Look for parasitized red blood cells.
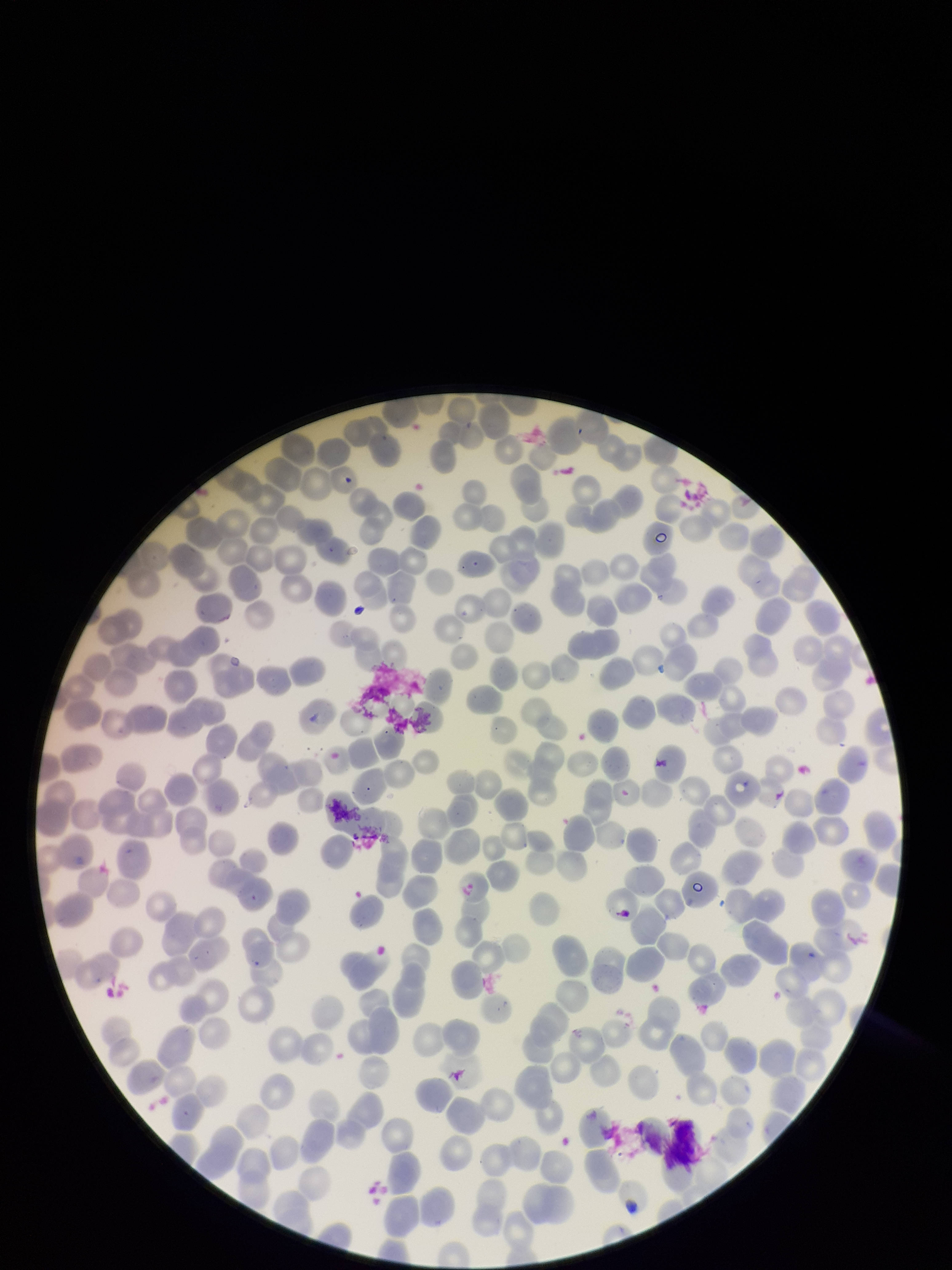
None detected.

Red blood cell count: 248. Giemsa stain. Parasitized red blood cell count: 0. Patient malaria status: negative. Image is 952×1270 pixels. Smartphone photograph taken through the eyepiece of a microscope. Preparation: thin. One field from this slide.